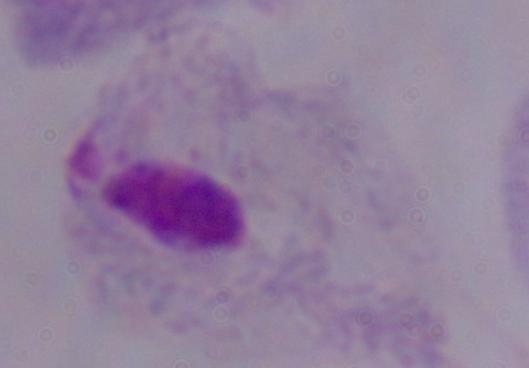
Photomicrograph. A trichomonad is shown. 1000x magnification.